Locate every Plasmodium parasite.
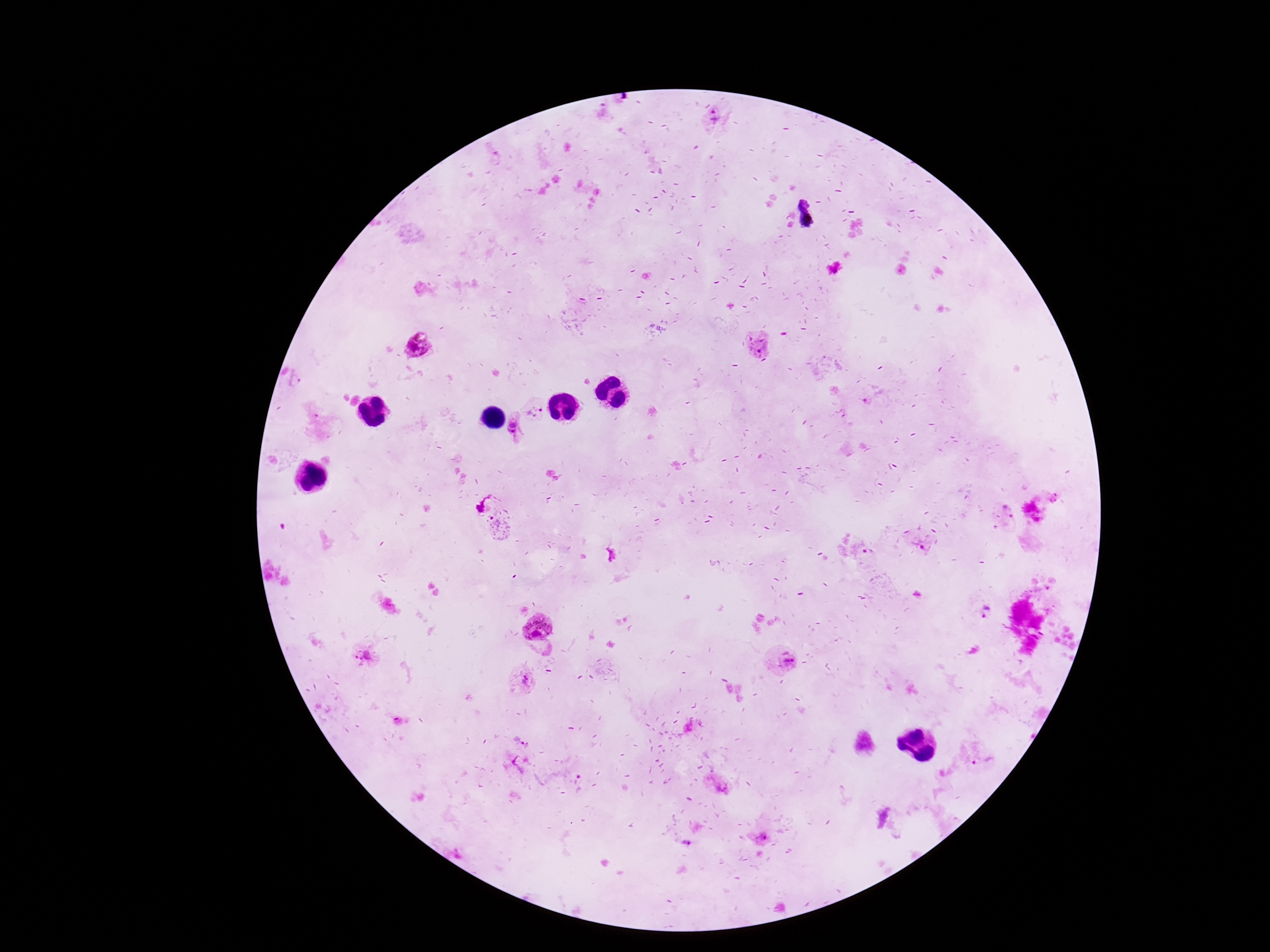

Approximate centers as (x, y) in pixels.
Plasmodium parasites: (417, 347), (762, 348), (534, 411), (515, 427), (497, 521), (985, 613), (537, 627), (365, 656), (783, 661), (524, 682), (982, 760), (764, 836).

{
  "capture": "smartphone camera through the microscope eyepiece",
  "stain": "Giemsa",
  "patient_malaria_status": "positive",
  "preparation": "thick blood film",
  "field_of_view": "one from this slide",
  "magnification": "100x",
  "image_size": "1270×952 pixels"
}